Name the parasite shown.
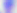

Toxoplasma gondii.

magnification = 400x
modality = photomicrograph